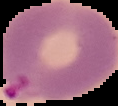

preparation = thin blood smear
image type = segmented cell region on a black background
malaria status = parasitized
image size = 118×106 pixels